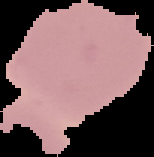

{
  "image_type": "segmented cell region with the area outside set to black",
  "result": "no Plasmodium parasites seen",
  "preparation": "thin blood smear",
  "image_size": "154×157 pixels"
}